Give the extent of all Plasmodium falciparum-infected red blood cells.
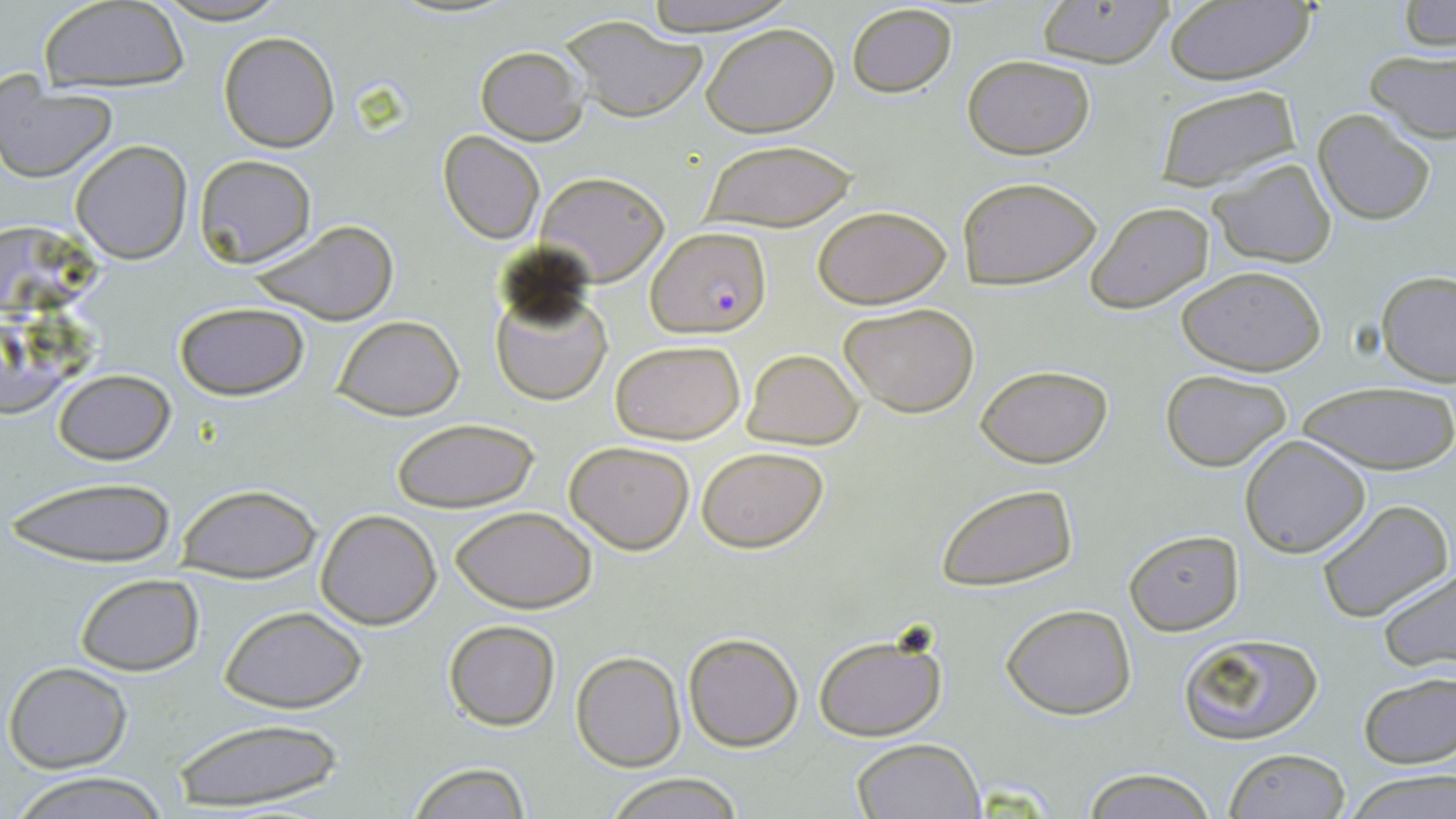

Approximate bounding boxes as named x1/y1/x2/y2 corners in pixels.
Plasmodium falciparum-infected red blood cells: (x1=647, y1=225, x2=770, y2=338).

slide-level diagnosis = Plasmodium falciparum
stain = May-Grünwald-Giemsa
magnification = 1000x
field of view = single
uninfected red blood cell locations = approximate bounding boxes as named x1/y1/x2/y2 corners in pixels: (x1=151, y1=0, x2=292, y2=24), (x1=639, y1=0, x2=798, y2=33), (x1=1162, y1=0, x2=1317, y2=87), (x1=39, y1=1, x2=190, y2=92), (x1=1034, y1=1, x2=1174, y2=69), (x1=1401, y1=2, x2=1456, y2=51), (x1=846, y1=3, x2=958, y2=98), (x1=559, y1=15, x2=708, y2=122), (x1=701, y1=23, x2=839, y2=137), (x1=219, y1=31, x2=341, y2=152), (x1=473, y1=45, x2=587, y2=145), (x1=1364, y1=47, x2=1456, y2=144), (x1=963, y1=54, x2=1095, y2=159), (x1=0, y1=82, x2=118, y2=181), (x1=1154, y1=84, x2=1302, y2=191), (x1=1311, y1=110, x2=1437, y2=225), (x1=438, y1=132, x2=545, y2=244), (x1=70, y1=139, x2=193, y2=264), (x1=699, y1=140, x2=858, y2=232), (x1=193, y1=154, x2=316, y2=267), (x1=1207, y1=158, x2=1336, y2=268), (x1=536, y1=170, x2=669, y2=286), (x1=957, y1=175, x2=1102, y2=290), (x1=1087, y1=202, x2=1214, y2=314), (x1=813, y1=205, x2=951, y2=309), (x1=244, y1=218, x2=400, y2=326), (x1=1, y1=220, x2=109, y2=317), (x1=1178, y1=265, x2=1326, y2=376), (x1=1377, y1=271, x2=1456, y2=386), (x1=490, y1=280, x2=612, y2=407), (x1=173, y1=301, x2=309, y2=402), (x1=839, y1=302, x2=981, y2=419), (x1=331, y1=316, x2=463, y2=420), (x1=1, y1=320, x2=100, y2=419), (x1=611, y1=340, x2=745, y2=445), (x1=743, y1=348, x2=863, y2=448), (x1=974, y1=362, x2=1114, y2=468), (x1=52, y1=368, x2=177, y2=465), (x1=1159, y1=369, x2=1292, y2=470), (x1=1297, y1=380, x2=1456, y2=476), (x1=390, y1=418, x2=542, y2=514), (x1=1240, y1=435, x2=1371, y2=557), (x1=564, y1=439, x2=695, y2=553), (x1=696, y1=446, x2=828, y2=553), (x1=8, y1=476, x2=177, y2=564), (x1=175, y1=483, x2=321, y2=583), (x1=935, y1=483, x2=1077, y2=591), (x1=1315, y1=498, x2=1453, y2=624), (x1=449, y1=506, x2=597, y2=613), (x1=315, y1=509, x2=441, y2=628), (x1=1124, y1=530, x2=1243, y2=637), (x1=1374, y1=566, x2=1456, y2=672), (x1=74, y1=574, x2=203, y2=674), (x1=1001, y1=603, x2=1137, y2=719), (x1=219, y1=605, x2=367, y2=712), (x1=443, y1=618, x2=562, y2=732), (x1=811, y1=631, x2=949, y2=742), (x1=683, y1=632, x2=803, y2=751), (x1=1178, y1=632, x2=1323, y2=746), (x1=571, y1=651, x2=685, y2=771), (x1=4, y1=661, x2=133, y2=772), (x1=1357, y1=672, x2=1455, y2=771), (x1=170, y1=717, x2=345, y2=813), (x1=850, y1=737, x2=984, y2=819), (x1=1224, y1=748, x2=1349, y2=819), (x1=407, y1=762, x2=532, y2=818), (x1=1080, y1=767, x2=1217, y2=819), (x1=1342, y1=767, x2=1456, y2=819), (x1=9, y1=771, x2=176, y2=819), (x1=603, y1=772, x2=744, y2=819)
image size = 1456×819 pixels
modality = light microscopy
preparation = thin blood film